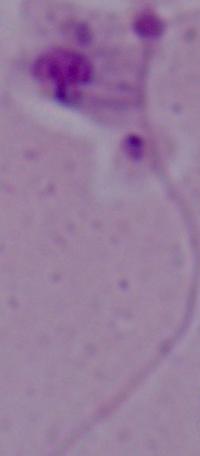

{
  "identification": "Leishmania",
  "modality": "micrograph",
  "magnification": "1000x"
}